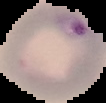
Image is 106×103 pixels. Segmented cell region on a black background. From a thin blood film. Result: Plasmodium parasites identified.